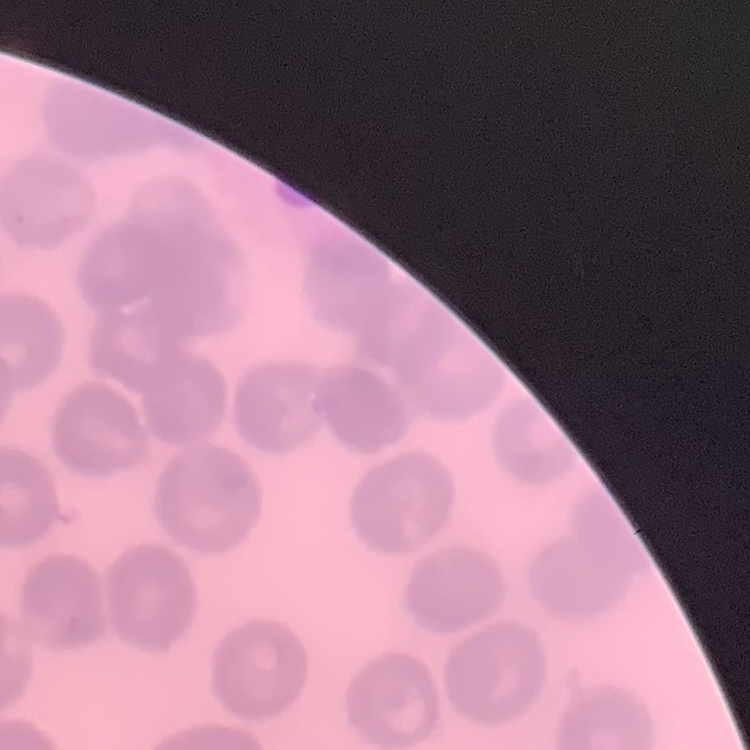
Summary:
  - Erythrocyte morphology: no rouleaux formation
  - Stain: Field's or Giemsa
  - Image type: square crop of a larger photomicrograph
  - Preparation: thin blood film